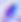
Captured at 400x magnification. Photomicrograph. Toxoplasma gondii is shown.